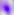
identification: Toxoplasma gondii
magnification: 400x
modality: micrograph